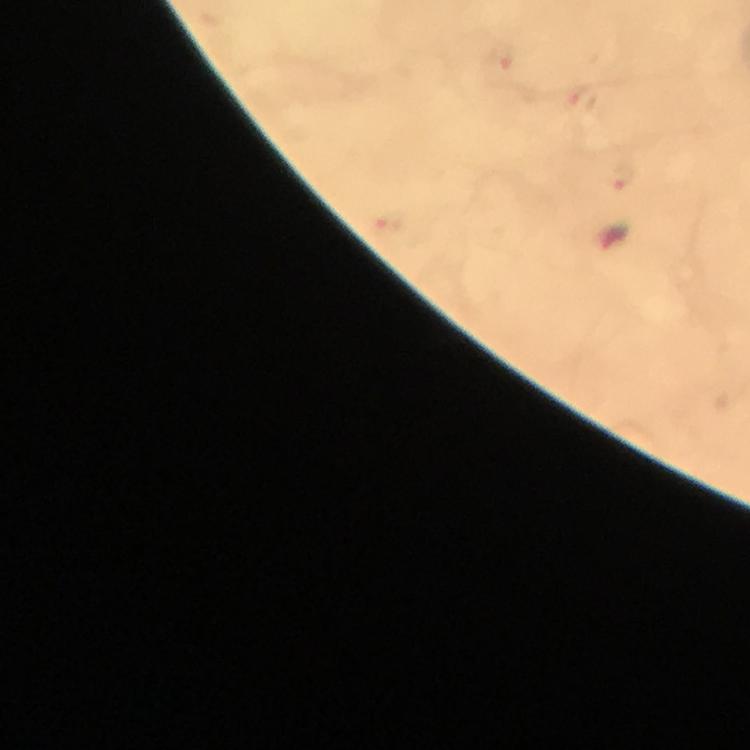

Approximate centers as [x, y] in pixels.
Summary:
  - Malaria parasite locations: [501, 68], [622, 176], [617, 239]
  - Context: from a diagnostic examination for malaria
  - Capture: smartphone photograph through a microscope
  - Magnification: 100x
  - Cropped from: a single field of view
  - Immersion oil: used
  - Image size: 750×750 pixels
  - Preparation: thick blood film
  - Stain: Giemsa